Classify this cell by malaria status.
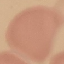

It is uninfected.

preparation = thin blood film
capture = smartphone camera at the microscope eyepiece
image type = cell patch, automatically extracted from a larger field of view and resized to 64 × 64 pixels
stain = Giemsa